Locate every blood parasite and identify its species.
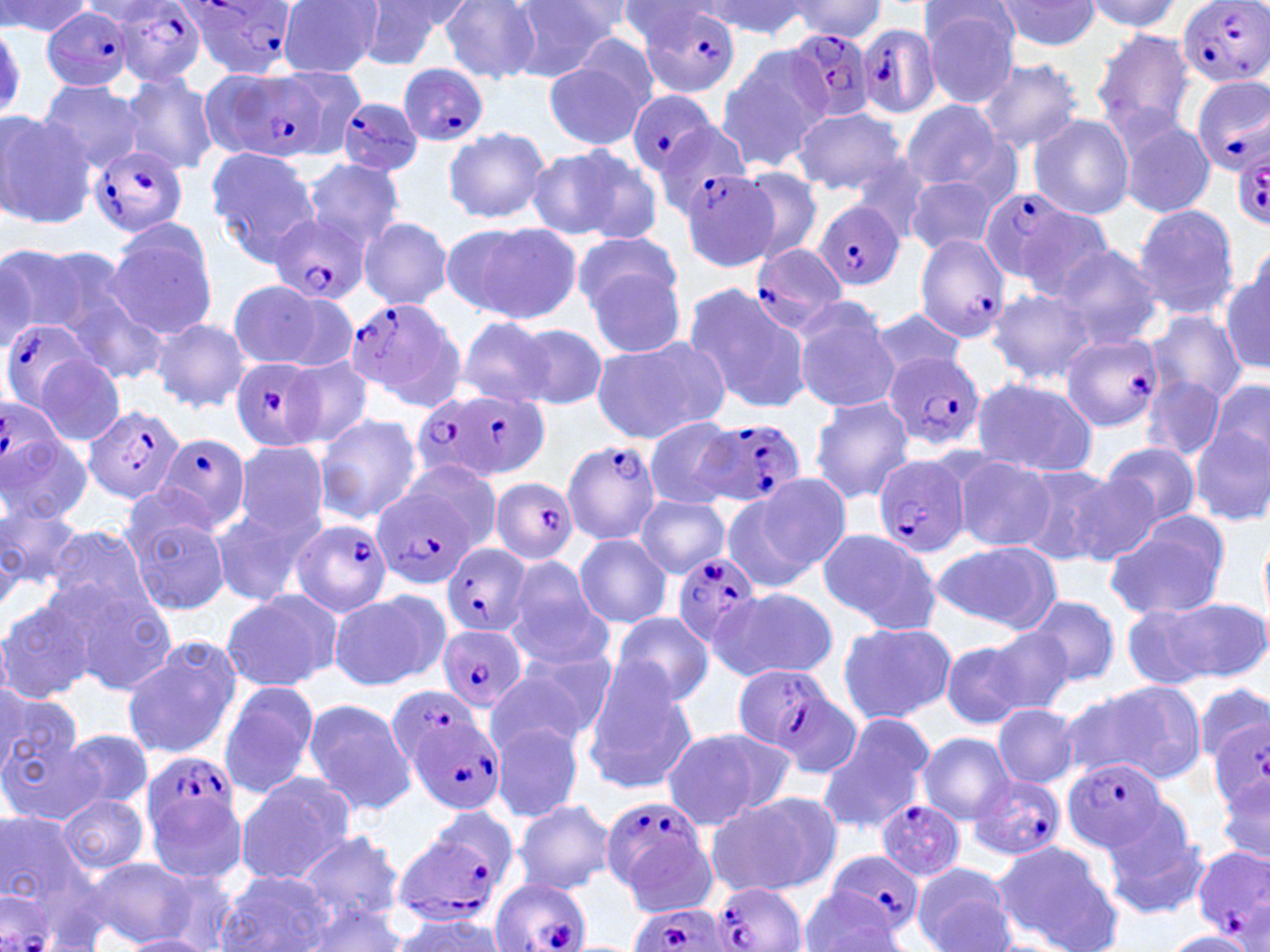

Approximate bounding boxes as named x1/y1/x2/y2 corners in pixels.
Plasmodium falciparum-infected red blood cells (subset): (x1=1176, y1=0, x2=1270, y2=89), (x1=181, y1=1, x2=299, y2=78), (x1=636, y1=4, x2=744, y2=99), (x1=109, y1=6, x2=208, y2=85), (x1=43, y1=8, x2=136, y2=92), (x1=856, y1=23, x2=941, y2=120), (x1=785, y1=29, x2=877, y2=124), (x1=397, y1=63, x2=491, y2=146), (x1=227, y1=68, x2=324, y2=164), (x1=1190, y1=76, x2=1270, y2=177), (x1=625, y1=89, x2=721, y2=179), (x1=334, y1=96, x2=424, y2=177), (x1=650, y1=119, x2=755, y2=218), (x1=1233, y1=142, x2=1270, y2=227), (x1=89, y1=144, x2=190, y2=237), (x1=978, y1=186, x2=1091, y2=292), (x1=815, y1=202, x2=904, y2=289), (x1=267, y1=214, x2=368, y2=306), (x1=914, y1=233, x2=1010, y2=343), (x1=748, y1=244, x2=849, y2=336), (x1=343, y1=299, x2=463, y2=407), (x1=1, y1=317, x2=100, y2=415), (x1=1060, y1=334, x2=1162, y2=433), (x1=882, y1=350, x2=986, y2=453), (x1=228, y1=356, x2=325, y2=451), (x1=416, y1=386, x2=546, y2=487), (x1=0, y1=399, x2=61, y2=500), (x1=84, y1=403, x2=184, y2=504), (x1=698, y1=417, x2=808, y2=510), (x1=154, y1=435, x2=251, y2=533), (x1=563, y1=441, x2=664, y2=545), (x1=873, y1=456, x2=970, y2=555), (x1=490, y1=477, x2=578, y2=564), (x1=373, y1=487, x2=477, y2=588), (x1=290, y1=519, x2=391, y2=616), (x1=441, y1=542, x2=530, y2=639), (x1=671, y1=554, x2=762, y2=648), (x1=437, y1=625, x2=528, y2=714), (x1=729, y1=662, x2=850, y2=769), (x1=398, y1=704, x2=507, y2=815), (x1=1208, y1=716, x2=1270, y2=838), (x1=1061, y1=758, x2=1168, y2=853), (x1=969, y1=773, x2=1066, y2=862), (x1=596, y1=793, x2=716, y2=907), (x1=875, y1=799, x2=965, y2=878), (x1=390, y1=808, x2=521, y2=927), (x1=1192, y1=845, x2=1270, y2=945), (x1=824, y1=848, x2=926, y2=938), (x1=491, y1=878, x2=592, y2=952), (x1=712, y1=880, x2=805, y2=952), (x1=0, y1=893, x2=58, y2=952), (x1=624, y1=905, x2=728, y2=952).
No Plasmodium ovale, Plasmodium malariae, Plasmodium vivax, Babesia divergens, or Trypanosoma brucei observed.

Uninfected red blood cell locations (subset): (x1=276, y1=0, x2=385, y2=76), (x1=615, y1=0, x2=720, y2=48), (x1=701, y1=0, x2=813, y2=39), (x1=995, y1=0, x2=1104, y2=51), (x1=1080, y1=0, x2=1184, y2=33), (x1=0, y1=1, x2=94, y2=37), (x1=441, y1=1, x2=542, y2=83), (x1=510, y1=1, x2=618, y2=81), (x1=784, y1=1, x2=888, y2=40), (x1=351, y1=2, x2=461, y2=70), (x1=921, y1=5, x2=1021, y2=107), (x1=1091, y1=27, x2=1199, y2=138), (x1=714, y1=46, x2=830, y2=172), (x1=544, y1=55, x2=649, y2=152), (x1=978, y1=58, x2=1084, y2=153), (x1=277, y1=66, x2=368, y2=156), (x1=119, y1=74, x2=219, y2=176), (x1=36, y1=78, x2=143, y2=175), (x1=897, y1=99, x2=1010, y2=196), (x1=790, y1=108, x2=911, y2=193), (x1=0, y1=110, x2=95, y2=230), (x1=1028, y1=113, x2=1135, y2=220), (x1=1116, y1=116, x2=1216, y2=218), (x1=442, y1=126, x2=549, y2=224), (x1=526, y1=142, x2=659, y2=245), (x1=205, y1=146, x2=321, y2=266), (x1=300, y1=157, x2=408, y2=254), (x1=733, y1=166, x2=824, y2=266), (x1=679, y1=170, x2=780, y2=270), (x1=904, y1=175, x2=1002, y2=257), (x1=1131, y1=204, x2=1240, y2=320), (x1=359, y1=217, x2=454, y2=309), (x1=103, y1=220, x2=220, y2=341), (x1=444, y1=220, x2=583, y2=327), (x1=571, y1=230, x2=684, y2=321), (x1=1, y1=242, x2=129, y2=348), (x1=1053, y1=244, x2=1163, y2=350), (x1=0, y1=251, x2=38, y2=351), (x1=584, y1=262, x2=688, y2=359), (x1=1220, y1=265, x2=1270, y2=375), (x1=226, y1=281, x2=341, y2=369), (x1=683, y1=283, x2=808, y2=416), (x1=986, y1=287, x2=1096, y2=385), (x1=68, y1=293, x2=170, y2=386), (x1=791, y1=305, x2=899, y2=414), (x1=869, y1=306, x2=966, y2=383), (x1=1147, y1=311, x2=1247, y2=407), (x1=457, y1=316, x2=555, y2=408), (x1=149, y1=318, x2=252, y2=413), (x1=515, y1=324, x2=608, y2=408), (x1=590, y1=338, x2=730, y2=445), (x1=34, y1=352, x2=126, y2=447), (x1=285, y1=354, x2=374, y2=450), (x1=1139, y1=373, x2=1225, y2=462), (x1=971, y1=376, x2=1099, y2=479), (x1=1204, y1=376, x2=1270, y2=478), (x1=808, y1=396, x2=915, y2=502), (x1=314, y1=413, x2=422, y2=524), (x1=641, y1=416, x2=740, y2=510), (x1=1192, y1=423, x2=1269, y2=525), (x1=229, y1=440, x2=331, y2=552), (x1=1099, y1=441, x2=1202, y2=528), (x1=0, y1=445, x2=93, y2=530), (x1=950, y1=452, x2=1055, y2=552), (x1=398, y1=460, x2=504, y2=557), (x1=1013, y1=463, x2=1123, y2=565), (x1=1064, y1=470, x2=1163, y2=567), (x1=753, y1=472, x2=852, y2=577), (x1=720, y1=487, x2=824, y2=593), (x1=634, y1=495, x2=729, y2=578), (x1=0, y1=498, x2=85, y2=601), (x1=210, y1=500, x2=313, y2=610), (x1=126, y1=509, x2=229, y2=616), (x1=1104, y1=514, x2=1232, y2=621), (x1=43, y1=526, x2=158, y2=625), (x1=1259, y1=526, x2=1270, y2=625), (x1=817, y1=528, x2=944, y2=633), (x1=574, y1=533, x2=673, y2=629), (x1=931, y1=539, x2=1063, y2=635), (x1=503, y1=553, x2=616, y2=678), (x1=51, y1=576, x2=177, y2=694), (x1=711, y1=587, x2=837, y2=681), (x1=329, y1=588, x2=448, y2=691), (x1=220, y1=589, x2=341, y2=694), (x1=0, y1=595, x2=101, y2=704), (x1=1029, y1=596, x2=1119, y2=686), (x1=1152, y1=597, x2=1268, y2=686), (x1=1118, y1=602, x2=1223, y2=690), (x1=610, y1=610, x2=714, y2=707), (x1=835, y1=620, x2=957, y2=725), (x1=981, y1=625, x2=1074, y2=716), (x1=121, y1=640, x2=241, y2=760), (x1=941, y1=640, x2=1030, y2=730), (x1=487, y1=657, x2=608, y2=756), (x1=580, y1=660, x2=701, y2=794), (x1=218, y1=680, x2=321, y2=800), (x1=1193, y1=681, x2=1268, y2=768), (x1=1061, y1=682, x2=1200, y2=784), (x1=0, y1=686, x2=80, y2=780), (x1=300, y1=698, x2=418, y2=815), (x1=992, y1=704, x2=1079, y2=788), (x1=818, y1=711, x2=937, y2=837), (x1=0, y1=720, x2=102, y2=827), (x1=489, y1=720, x2=583, y2=822), (x1=659, y1=725, x2=793, y2=831), (x1=61, y1=728, x2=155, y2=813), (x1=917, y1=732, x2=1015, y2=824), (x1=234, y1=772, x2=358, y2=885), (x1=706, y1=792, x2=838, y2=897), (x1=58, y1=793, x2=150, y2=874), (x1=511, y1=798, x2=614, y2=894), (x1=1099, y1=804, x2=1209, y2=920), (x1=1, y1=805, x2=108, y2=931), (x1=296, y1=829, x2=406, y2=926), (x1=991, y1=838, x2=1124, y2=952), (x1=85, y1=857, x2=197, y2=948), (x1=911, y1=865, x2=1018, y2=952), (x1=152, y1=869, x2=243, y2=952), (x1=218, y1=870, x2=337, y2=951), (x1=800, y1=888, x2=904, y2=952), (x1=297, y1=902, x2=410, y2=951), (x1=387, y1=913, x2=508, y2=951), (x1=1158, y1=930, x2=1259, y2=951), (x1=123, y1=935, x2=213, y2=951). Slide-level diagnosis: Plasmodium falciparum. One field of a larger specimen. Captured at 1000x magnification. Optical microscopy. Image is 1270×952 pixels. Thin blood film. May-Grünwald-Giemsa-stained preparation.